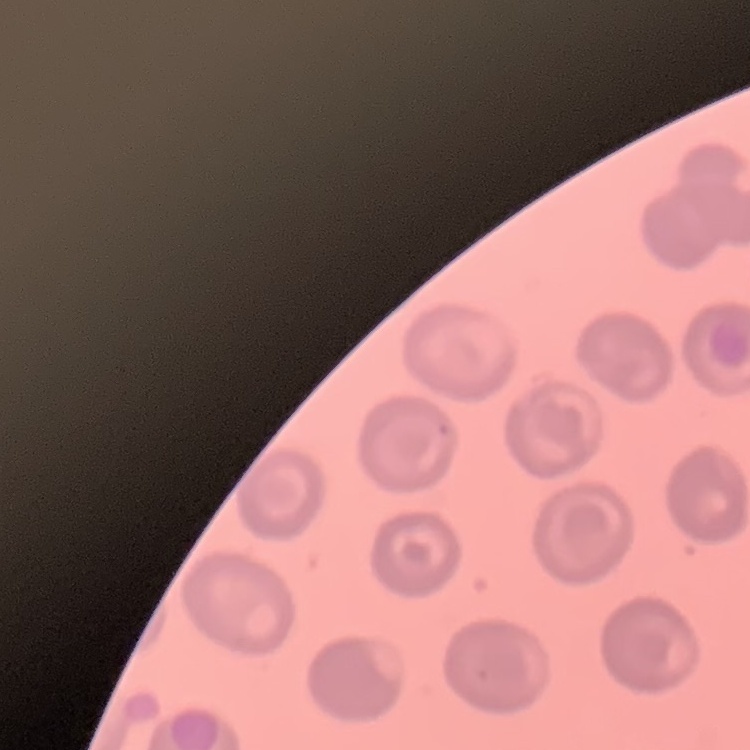

The erythrocytes exhibit no rouleaux formation. Thin blood film. Square crop of a larger photomicrograph. Field's or Giemsa stain.